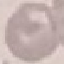

malaria status = uninfected
image type = cell patch, automatically extracted from a larger field of view and resized to 64 × 64 pixels
stain = Giemsa
preparation = thin smear
capture = smartphone camera at the microscope eyepiece